Comment on the morphology of the red blood cells.
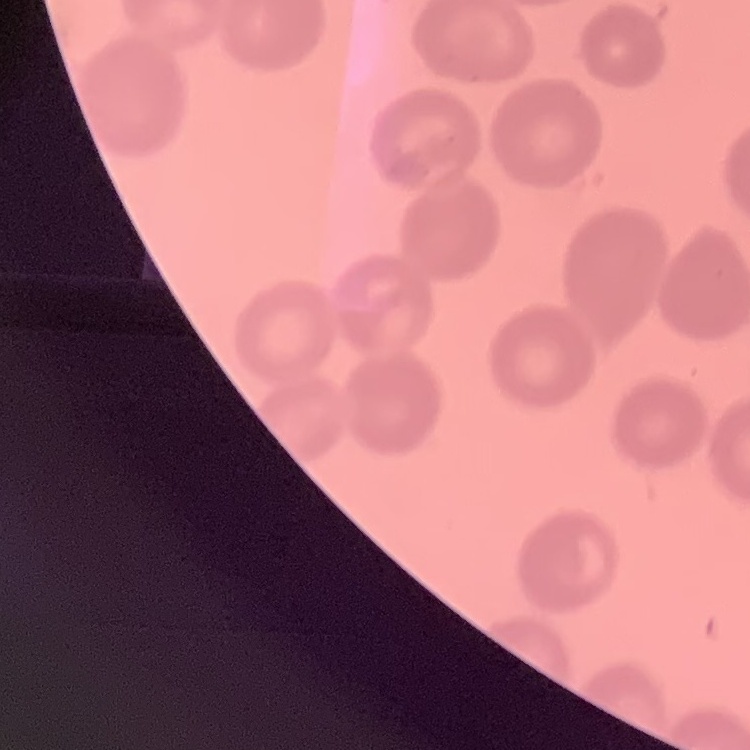

They show no rouleaux formation.

Summary:
  - Image type: one tile cut from a larger photomicrograph
  - Preparation: thin blood film
  - Stain: Field's or Giemsa